Assess this cell for malaria.
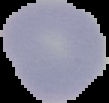

Uninfected.

Image is 109×103 pixels. From a thin blood film. Segmented cell region on a black background.